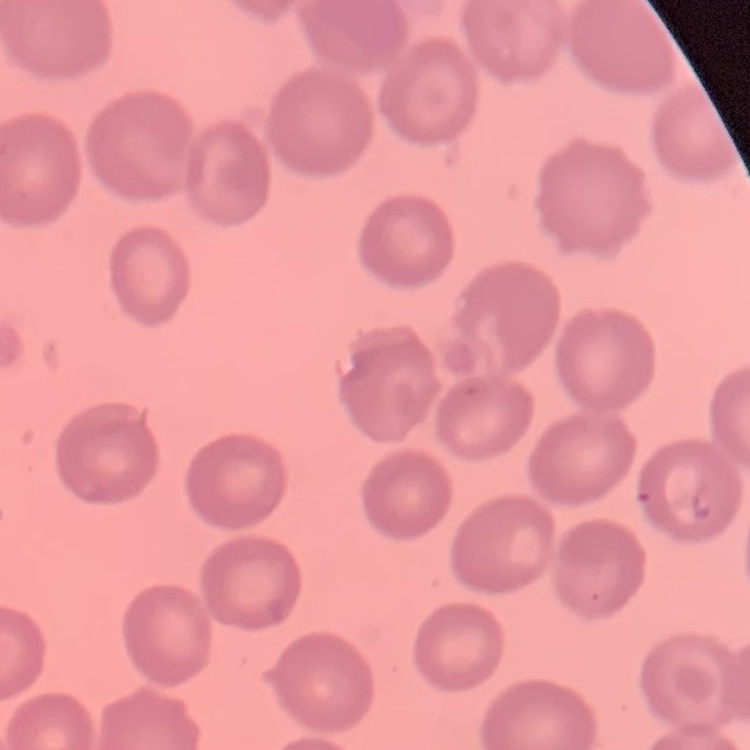
Summary:
  - Red blood cell morphology: no rouleaux formation
  - Preparation: thin blood film
  - Stain: Field's or Giemsa
  - Image type: one tile cut from a larger photomicrograph